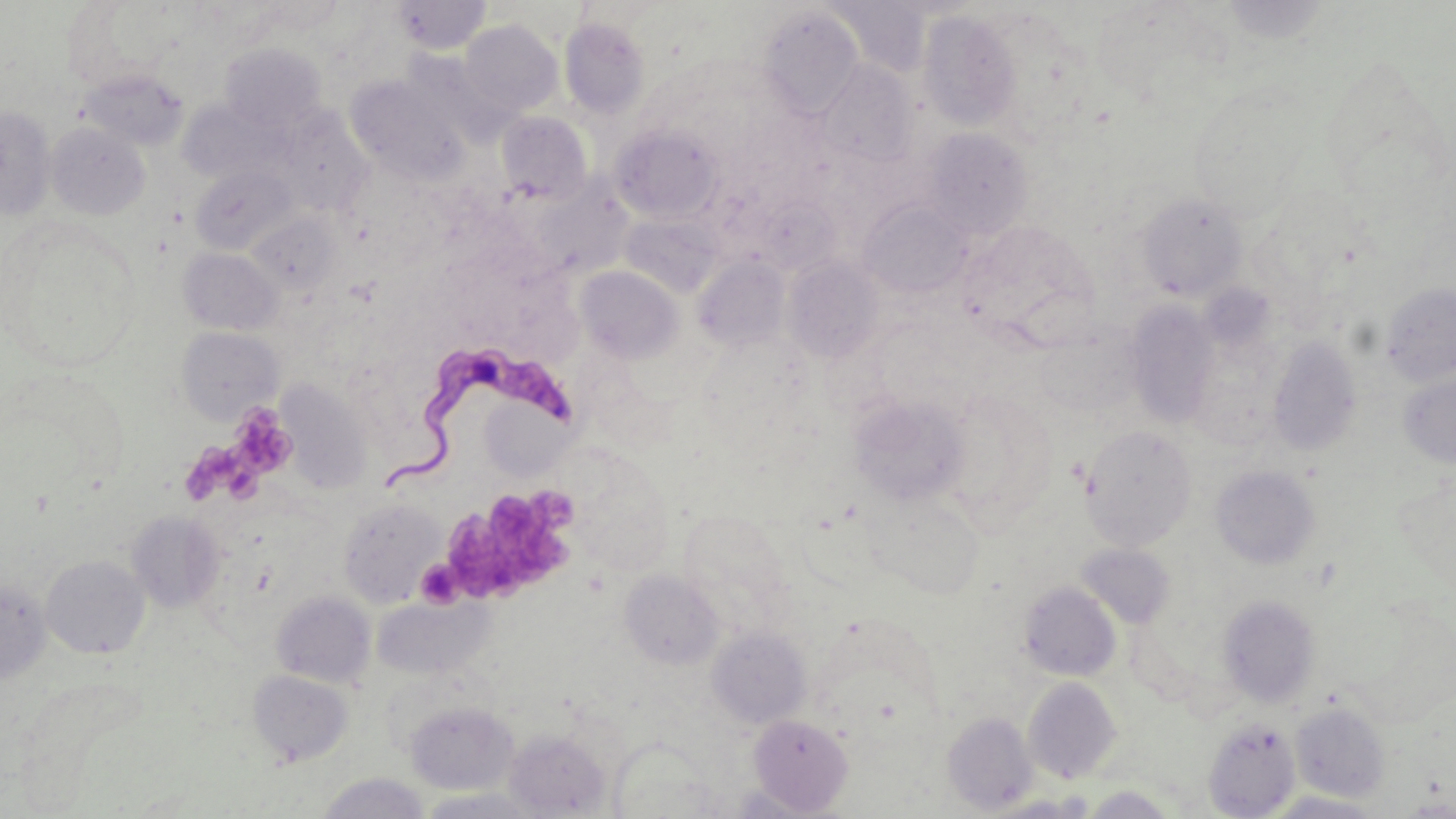

Summary:
  - Coordinate format: approximate bounding boxes as [x1, y1, x2, y2] in pixels
  - Trypanosoma brucei locations: [381, 342, 576, 493]
  - Platelet locations: [229, 408, 298, 480], [188, 440, 269, 506], [440, 487, 577, 607]
  - Uninfected red blood cell locations: [254, 0, 348, 33], [392, 0, 492, 54], [1219, 0, 1333, 45], [61, 1, 174, 93], [826, 3, 932, 79], [1095, 5, 1212, 98], [758, 7, 863, 118], [917, 9, 1023, 132], [559, 17, 651, 119], [460, 19, 562, 116], [219, 43, 327, 136], [1318, 54, 1451, 204], [816, 60, 918, 168], [78, 67, 189, 151], [345, 74, 469, 185], [179, 100, 283, 184], [0, 106, 56, 220], [278, 111, 372, 214], [496, 112, 592, 205], [46, 122, 149, 220], [611, 125, 722, 223], [921, 128, 1033, 239], [191, 166, 295, 253], [532, 182, 632, 276], [1136, 191, 1249, 302], [755, 196, 839, 273], [859, 201, 972, 298], [247, 212, 340, 294], [622, 214, 723, 298], [957, 220, 1102, 353], [0, 221, 139, 372], [179, 247, 281, 334], [693, 255, 792, 353], [784, 257, 884, 363], [576, 265, 684, 363], [1380, 283, 1456, 386], [1124, 301, 1220, 429], [176, 327, 283, 425], [1036, 328, 1138, 417], [1267, 337, 1362, 458], [1398, 372, 1456, 468], [278, 381, 372, 494], [484, 391, 575, 482], [849, 394, 972, 507], [1080, 425, 1198, 551], [562, 449, 673, 575], [1211, 465, 1320, 571], [1398, 478, 1456, 599], [860, 489, 985, 598], [338, 497, 444, 607], [126, 510, 225, 613], [1076, 543, 1176, 629], [41, 554, 149, 659], [619, 570, 725, 671], [0, 578, 50, 684], [1018, 581, 1121, 681], [271, 591, 376, 688], [1218, 594, 1321, 707], [373, 595, 492, 680], [707, 627, 812, 729], [247, 670, 353, 766], [1022, 677, 1123, 783], [405, 701, 518, 795], [1290, 702, 1390, 801], [943, 712, 1038, 814], [748, 713, 854, 815], [1202, 718, 1300, 818], [504, 730, 611, 817], [317, 772, 430, 818], [1081, 786, 1179, 818], [415, 788, 544, 818], [1265, 791, 1384, 818], [984, 793, 1097, 818], [1399, 798, 1456, 817]
  - Slide-level diagnosis: Trypanosoma brucei
  - Modality: optical microscopy
  - Field of view: single
  - Image size: 1456×819 pixels
  - Stain: May-Grünwald-Giemsa
  - Magnification: 1000x
  - Preparation: thin blood film